Identify the parasite.
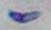

Toxoplasma gondii.

Summary:
  - Magnification: 1000x
  - Modality: photomicrograph